Assess this cell for malaria.
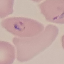

Parasitized.

Summary:
  - Capture: smartphone through the microscope eyepiece
  - Stain: Giemsa
  - Preparation: thin blood film
  - Image type: automatically extracted cell patch, resized to 64 × 64 pixels